Assess the morphology of the red blood cells.
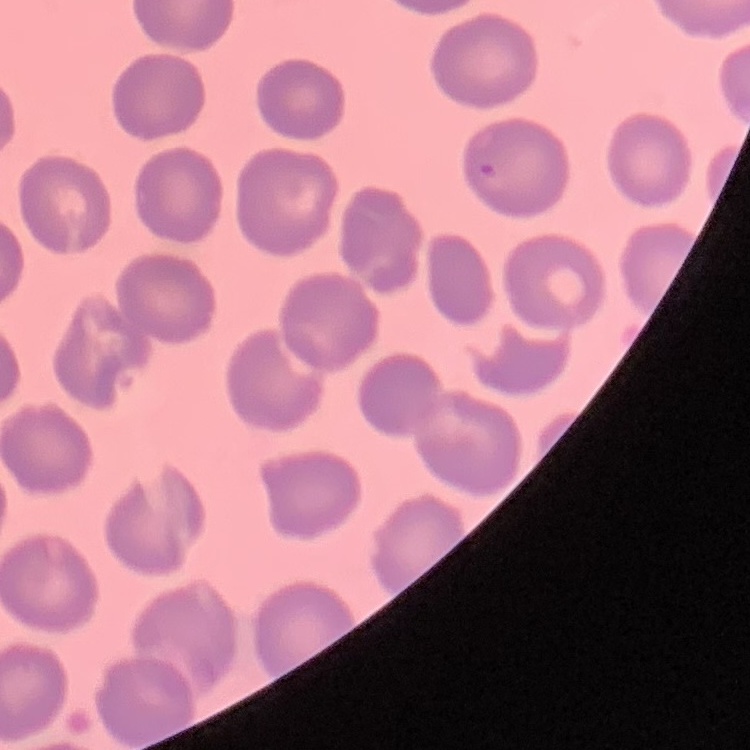
No rouleaux formation.

stain = Field's or Giemsa
preparation = thin blood smear
image type = square crop of a larger photomicrograph